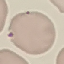
{
  "result": "no malaria parasites detected",
  "stain": "Giemsa",
  "capture": "smartphone camera at the microscope eyepiece",
  "image_type": "automatically extracted cell patch, resized to 64 × 64 pixels",
  "preparation": "thin blood smear"
}